Assess the morphology of the red blood cells.
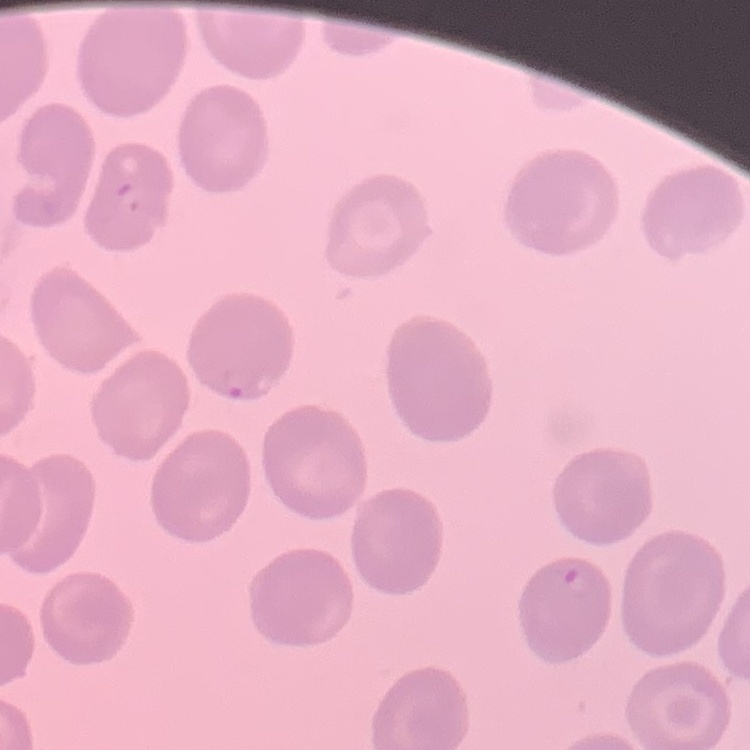
No rouleaux formation.

preparation = thin blood film
image type = square crop of a larger photomicrograph
stain = Field's or Giemsa